Outline every Plasmodium parasite.
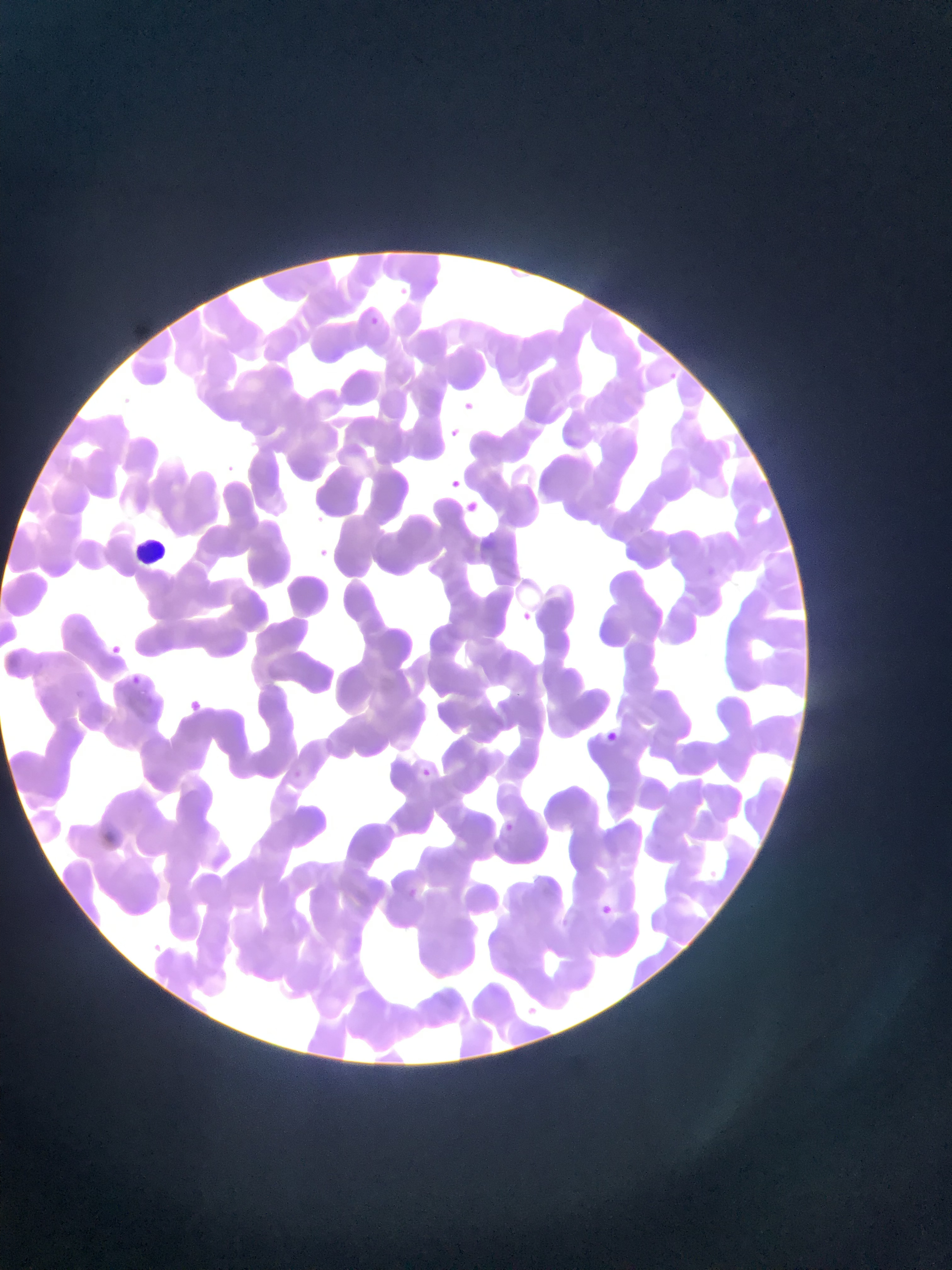

Approximate bounding boxes as (left, top, right, bottom) in pixels.
Plasmodium parasites: (397, 284, 408, 296), (370, 313, 382, 330), (667, 368, 677, 379), (119, 389, 142, 413), (453, 394, 484, 418), (436, 424, 456, 437), (215, 453, 247, 479), (452, 477, 466, 491), (470, 499, 487, 514), (306, 510, 328, 524), (319, 546, 338, 560), (705, 564, 729, 584), (521, 609, 540, 625), (104, 635, 124, 658), (132, 676, 140, 684), (189, 688, 206, 718), (605, 728, 625, 749), (419, 764, 440, 787), (283, 765, 314, 783), (498, 812, 521, 835), (409, 887, 420, 903), (599, 902, 619, 916), (152, 945, 167, 967), (524, 999, 550, 1028).

Summary:
  - Leukocyte locations: (132, 531, 187, 569)
  - Preparation: thin blood film
  - Country: Ghana
  - Image size: 952×1270 pixels
  - Capture: mobile-phone photograph through a microscope
  - Field of view: single